Assess for Plasmodium parasites.
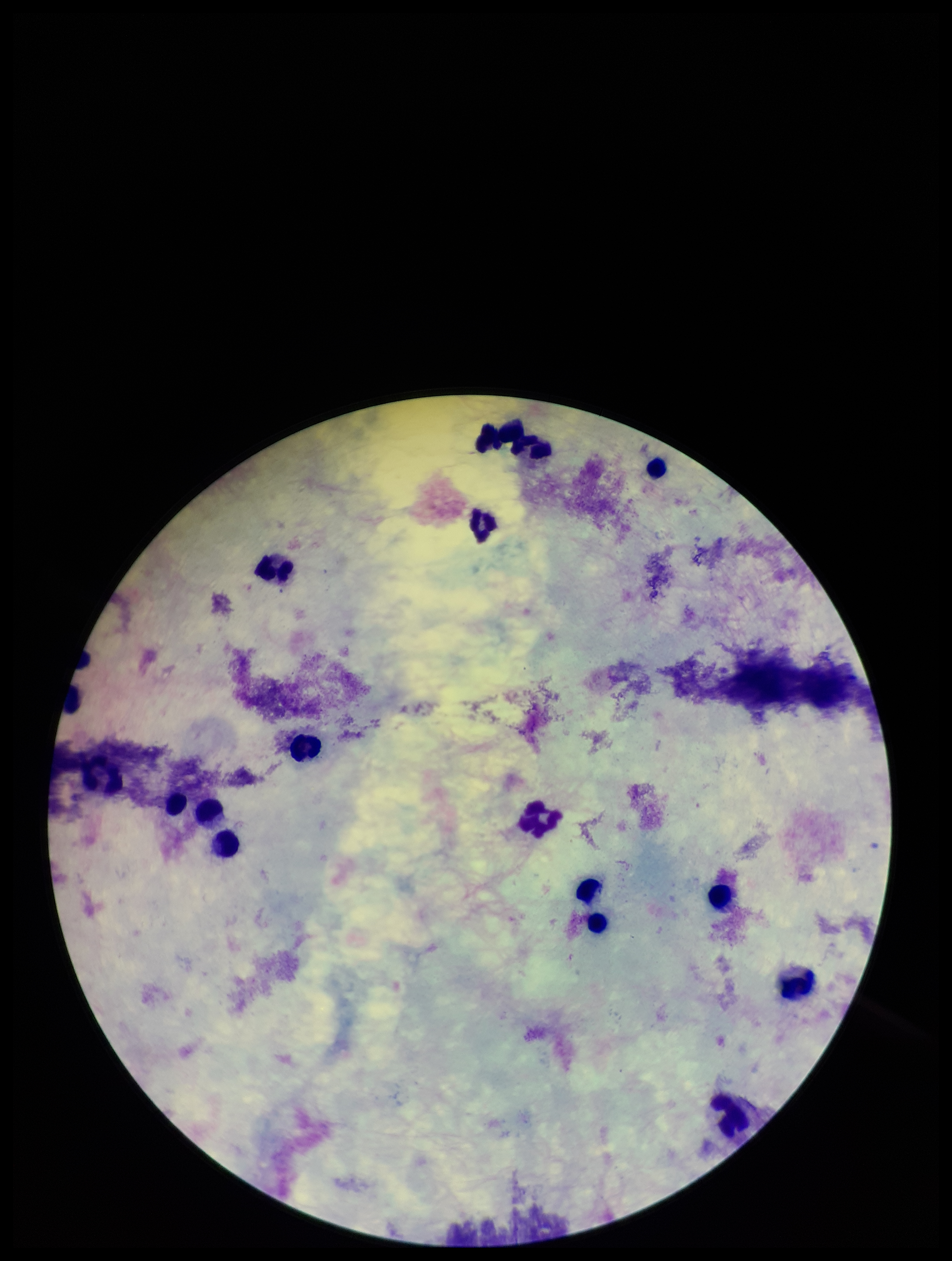

None detected.

Giemsa stain. Leukocyte count: 16. One field from this slide. Preparation: thick smear. Parasite count: 0. Image is 952×1261 pixels. Patient malaria status: negative. Photographed through the microscope eyepiece with a smartphone camera.